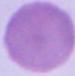 A red blood cell is seen. 1000x magnification. Photomicrograph.